Assess for malaria.
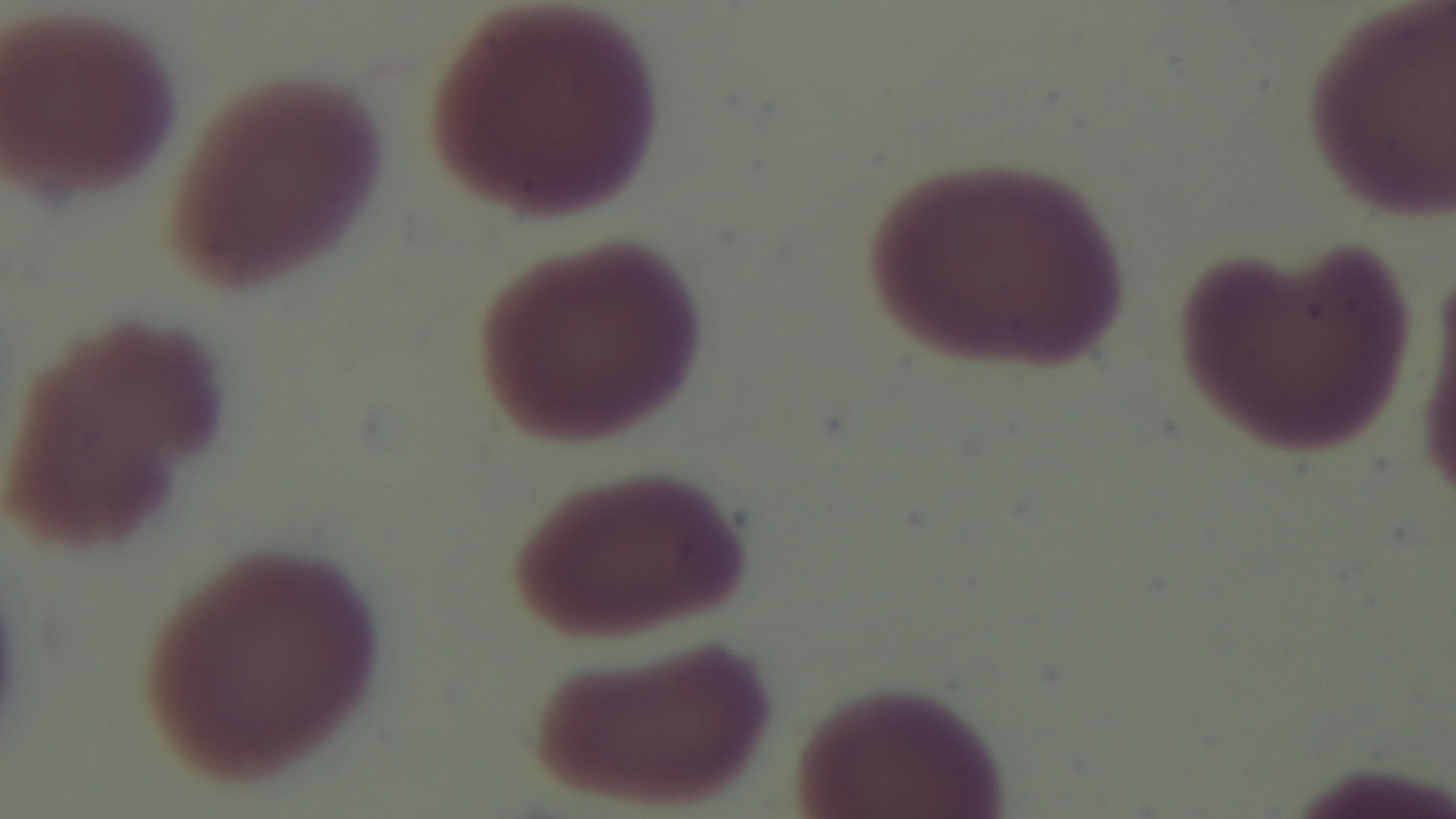

It is uninfected.

Light microscopy. Preparation: thin blood film. Captured with a mounted 4K digital camera. One field from the slide. 100x oil-immersion objective. Giemsa stain.